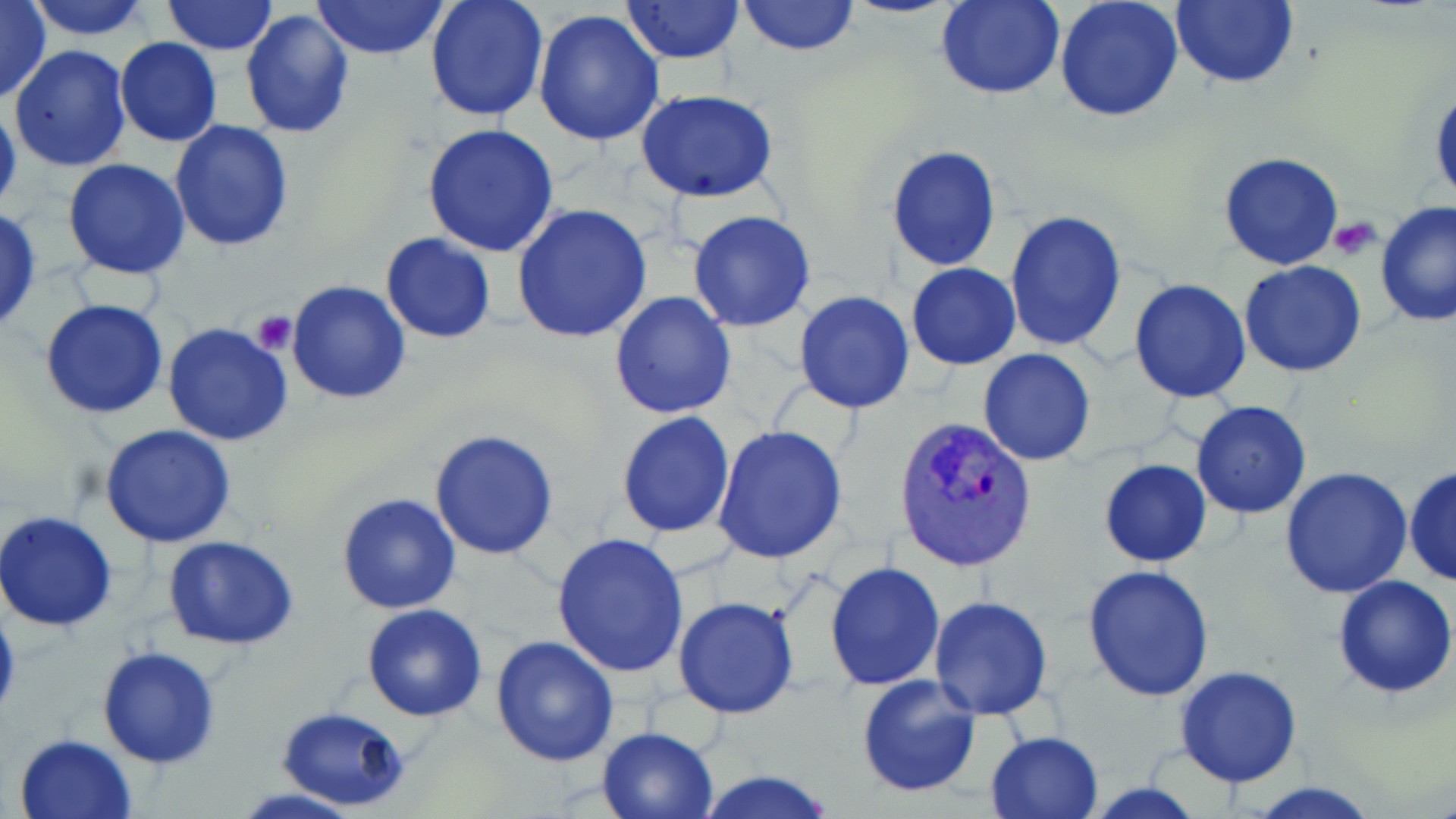

{
  "plasmodium_vivax_infected_red_blood_cell_locations": "approximate bounding boxes as named x1/y1/x2/y2 corners in pixels: (x1=893, y1=416, x2=1036, y2=574)",
  "slide_level_diagnosis": "Plasmodium vivax",
  "stain": "May-Grünwald-Giemsa",
  "platelet_locations": "approximate bounding boxes as named x1/y1/x2/y2 corners in pixels: (x1=1329, y1=217, x2=1383, y2=256), (x1=250, y1=308, x2=298, y2=354)",
  "uninfected_red_blood_cell_locations": "approximate bounding boxes as named x1/y1/x2/y2 corners in pixels: (x1=0, y1=0, x2=51, y2=105), (x1=26, y1=0, x2=155, y2=39), (x1=312, y1=0, x2=448, y2=60), (x1=425, y1=0, x2=548, y2=122), (x1=623, y1=0, x2=745, y2=65), (x1=938, y1=0, x2=1065, y2=99), (x1=1055, y1=0, x2=1184, y2=122), (x1=1171, y1=0, x2=1297, y2=89), (x1=162, y1=1, x2=278, y2=54), (x1=737, y1=1, x2=859, y2=55), (x1=240, y1=8, x2=355, y2=138), (x1=532, y1=8, x2=666, y2=145), (x1=114, y1=37, x2=222, y2=147), (x1=9, y1=45, x2=130, y2=173), (x1=1430, y1=82, x2=1455, y2=211), (x1=638, y1=92, x2=777, y2=204), (x1=0, y1=99, x2=21, y2=218), (x1=169, y1=120, x2=294, y2=252), (x1=421, y1=124, x2=559, y2=257), (x1=886, y1=145, x2=1002, y2=272), (x1=1218, y1=152, x2=1345, y2=271), (x1=63, y1=158, x2=192, y2=280), (x1=1375, y1=199, x2=1456, y2=328), (x1=512, y1=203, x2=654, y2=343), (x1=0, y1=208, x2=43, y2=331), (x1=687, y1=209, x2=817, y2=331), (x1=1004, y1=210, x2=1126, y2=350), (x1=381, y1=233, x2=496, y2=343), (x1=1239, y1=261, x2=1368, y2=378), (x1=907, y1=263, x2=1020, y2=371), (x1=287, y1=279, x2=413, y2=403), (x1=1129, y1=279, x2=1251, y2=403), (x1=794, y1=290, x2=915, y2=414), (x1=609, y1=291, x2=737, y2=420), (x1=39, y1=299, x2=170, y2=420), (x1=162, y1=321, x2=295, y2=447), (x1=977, y1=349, x2=1096, y2=466), (x1=1190, y1=401, x2=1312, y2=519), (x1=616, y1=410, x2=736, y2=538), (x1=99, y1=423, x2=237, y2=547), (x1=714, y1=425, x2=847, y2=563), (x1=430, y1=428, x2=560, y2=560), (x1=1098, y1=457, x2=1211, y2=568), (x1=1405, y1=465, x2=1456, y2=587), (x1=1279, y1=466, x2=1413, y2=599), (x1=336, y1=490, x2=462, y2=615), (x1=0, y1=510, x2=118, y2=634), (x1=551, y1=532, x2=692, y2=676), (x1=162, y1=536, x2=300, y2=650), (x1=824, y1=561, x2=945, y2=689), (x1=1083, y1=564, x2=1215, y2=702), (x1=1332, y1=573, x2=1456, y2=699), (x1=673, y1=595, x2=800, y2=718), (x1=929, y1=596, x2=1054, y2=720), (x1=0, y1=598, x2=20, y2=730), (x1=360, y1=603, x2=488, y2=722), (x1=490, y1=634, x2=621, y2=767), (x1=97, y1=645, x2=221, y2=768), (x1=1174, y1=666, x2=1304, y2=787), (x1=855, y1=673, x2=983, y2=797), (x1=275, y1=705, x2=412, y2=813), (x1=596, y1=725, x2=721, y2=818), (x1=985, y1=730, x2=1104, y2=819), (x1=13, y1=732, x2=138, y2=819), (x1=694, y1=768, x2=840, y2=819), (x1=1240, y1=780, x2=1385, y2=818), (x1=224, y1=787, x2=376, y2=819)",
  "magnification": "1000x",
  "image_size": "1456×819 pixels",
  "field_of_view": "one of a larger specimen",
  "preparation": "thin blood film",
  "modality": "optical microscopy"
}